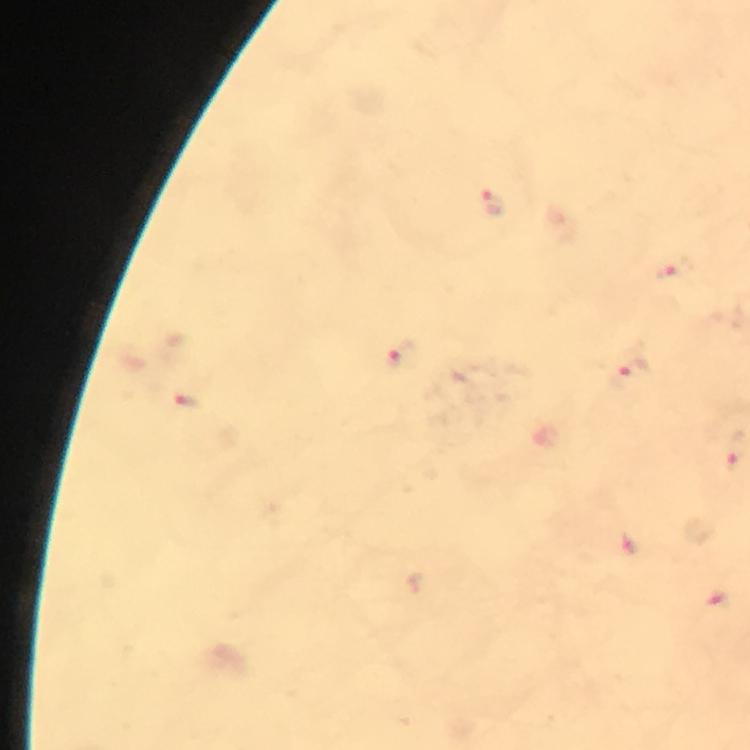 Approximate object centers, in pixels from the top-left corner. Plasmodium parasite locations: (x=493, y=203), (x=669, y=273), (x=403, y=356), (x=631, y=374), (x=188, y=401), (x=734, y=458). A crop from one field of view. Giemsa stain. Immersion oil was used. At 100x magnification. Thick blood smear. From a diagnostic examination for malaria. Smartphone photograph taken through a microscope. Image is 750×750 pixels.